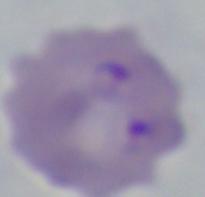
magnification: 1000x
modality: micrograph
identification: Babesia